Outline each blood parasite and name the species.
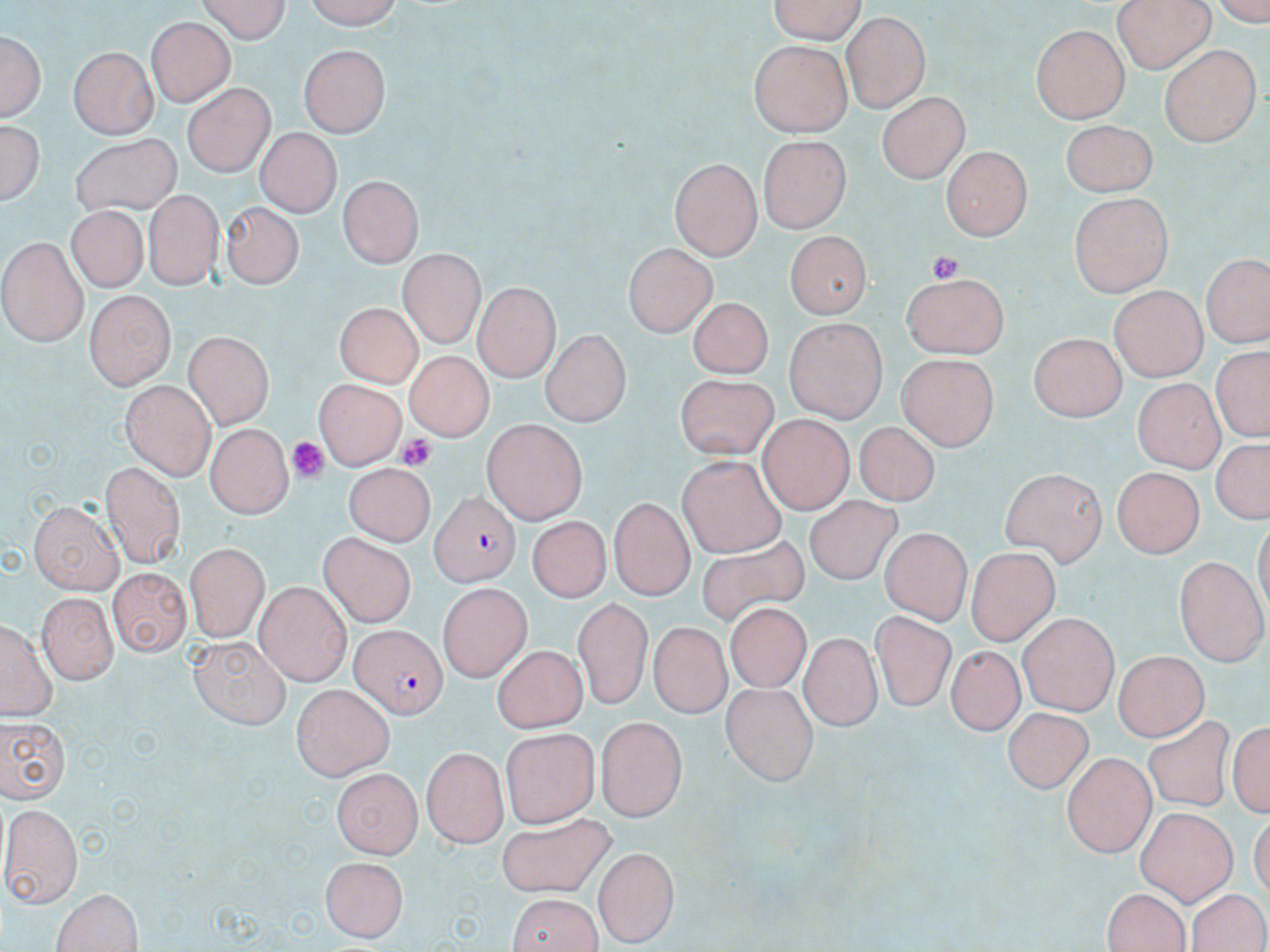
Approximate bounding boxes as (x1, y1, x2, y2) in pixels.
Plasmodium falciparum-infected red blood cells: (428, 488, 517, 583), (350, 622, 447, 719).
No Plasmodium ovale, Plasmodium malariae, Plasmodium vivax, Babesia divergens, or Trypanosoma brucei observed.

Platelet locations: (929, 252, 964, 284), (396, 431, 440, 470), (291, 438, 331, 480). Uninfected red blood cell locations: (194, 0, 292, 42), (302, 0, 405, 27), (765, 0, 867, 42), (1111, 0, 1215, 72), (1129, 7, 1237, 104), (842, 13, 931, 110), (145, 16, 235, 105), (1030, 25, 1131, 121), (1, 30, 46, 121), (748, 39, 849, 136), (1160, 41, 1258, 147), (298, 42, 390, 136), (70, 45, 159, 137), (183, 84, 273, 178), (878, 92, 967, 184), (2, 117, 44, 206), (1058, 119, 1157, 196), (256, 129, 338, 218), (74, 133, 184, 215), (758, 133, 849, 233), (941, 149, 1030, 240), (671, 158, 763, 260), (335, 173, 422, 268), (140, 189, 225, 287), (1068, 192, 1172, 295), (219, 201, 301, 292), (72, 202, 148, 287), (782, 232, 871, 320), (1, 236, 89, 345), (625, 247, 715, 335), (399, 251, 485, 350), (1202, 252, 1270, 349), (901, 270, 1008, 360), (472, 286, 557, 379), (1107, 286, 1209, 383), (84, 290, 174, 392), (686, 300, 774, 378), (334, 303, 424, 388), (781, 317, 886, 420), (540, 330, 632, 426), (1030, 330, 1131, 421), (185, 332, 274, 427), (1208, 345, 1268, 442), (893, 350, 994, 449), (403, 352, 493, 439), (669, 373, 777, 460), (316, 379, 403, 471), (1135, 379, 1222, 472), (120, 382, 217, 476), (759, 416, 854, 514), (481, 418, 586, 523), (852, 420, 938, 506), (206, 421, 296, 515), (1206, 440, 1268, 527), (673, 453, 786, 560), (103, 461, 187, 570), (345, 461, 428, 549), (1114, 468, 1204, 558), (999, 469, 1105, 568), (802, 495, 905, 584), (610, 500, 695, 599), (29, 503, 123, 595), (528, 514, 614, 600), (881, 527, 971, 622), (699, 533, 806, 625), (316, 534, 414, 629), (183, 545, 265, 640), (968, 548, 1061, 645), (1176, 554, 1268, 662), (107, 569, 188, 659), (255, 582, 352, 682), (439, 583, 529, 683), (37, 589, 116, 683), (573, 596, 652, 709), (727, 605, 811, 691), (1017, 612, 1118, 715), (869, 613, 955, 710), (3, 615, 52, 720), (648, 621, 733, 717), (800, 633, 879, 730), (189, 634, 291, 729), (491, 644, 585, 731), (941, 647, 1028, 733), (1111, 650, 1209, 740), (722, 681, 818, 785), (292, 682, 395, 778), (1003, 707, 1096, 795), (1143, 712, 1233, 811), (1230, 712, 1270, 824), (595, 714, 688, 821), (0, 716, 70, 804), (499, 728, 601, 824), (423, 746, 508, 846), (1062, 751, 1156, 855), (332, 768, 423, 855), (3, 802, 81, 904), (1135, 809, 1235, 904), (500, 811, 617, 894), (593, 846, 682, 944), (321, 857, 409, 940), (51, 887, 144, 952), (1101, 889, 1198, 950), (504, 892, 605, 952), (1189, 892, 1270, 952). Slide-level diagnosis: Plasmodium falciparum. Thin blood smear. Single field of view. 1000x magnification. Optical microscopy. Image is 1270×952 pixels. May-Grünwald-Giemsa-stained preparation.